Report the malaria status of this cell.
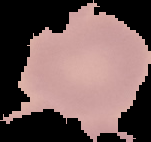

Uninfected.

Summary:
  - Preparation: thin blood film
  - Image size: 151×142 pixels
  - Image type: cell region segmented out of the field of view; surrounding area masked to black